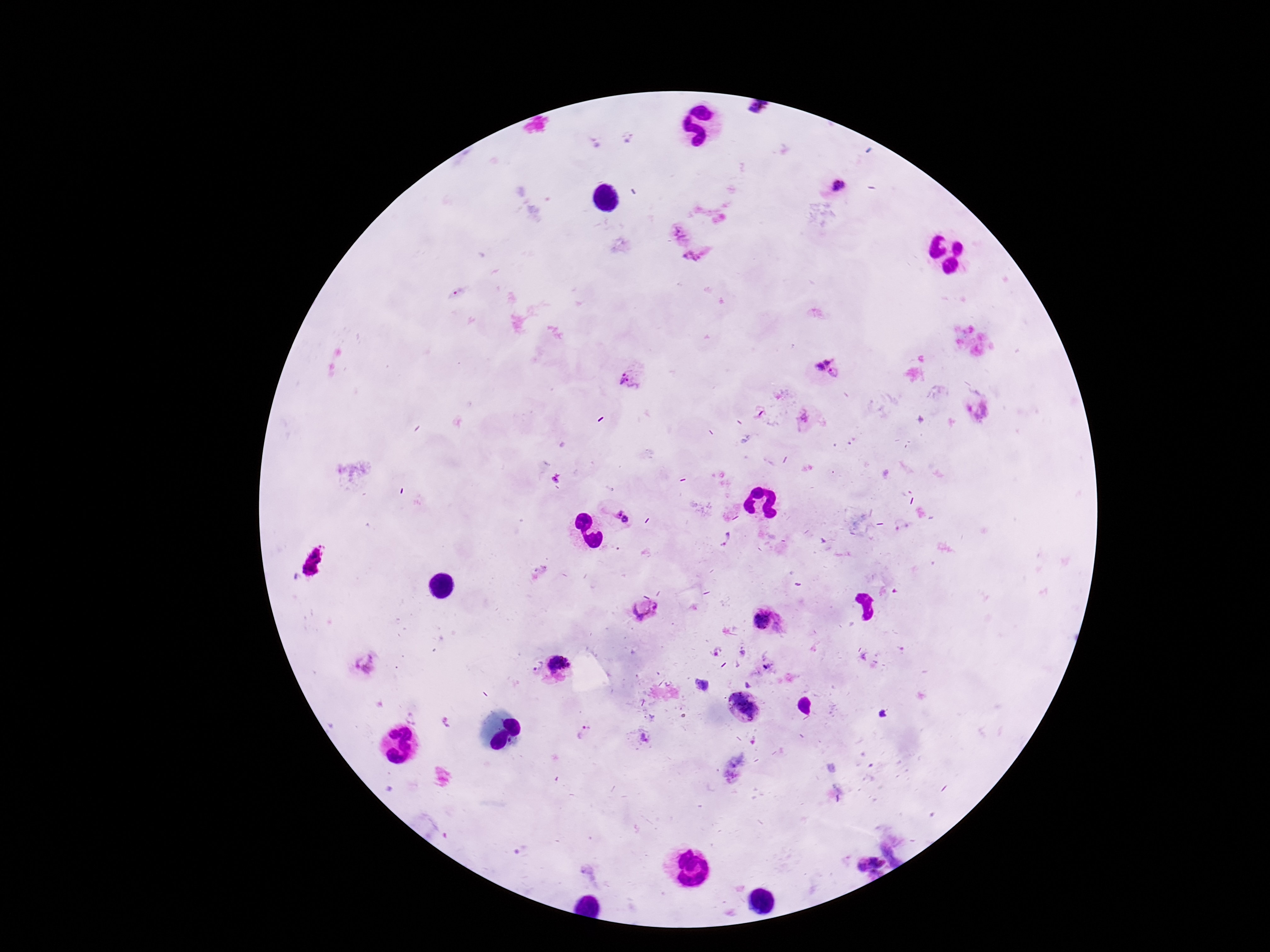

Approximate object centers, in pixels from the top-left corner. Plasmodium parasite locations: (x=836, y=186), (x=678, y=234), (x=697, y=259), (x=817, y=359), (x=838, y=374), (x=632, y=384), (x=805, y=419), (x=620, y=513), (x=644, y=609), (x=767, y=621), (x=365, y=664), (x=559, y=665), (x=531, y=666), (x=743, y=706), (x=586, y=734), (x=643, y=740), (x=867, y=860). Smartphone photograph taken through the microscope eyepiece. Thick peripheral-blood smear. Giemsa stain. 100x magnification. Patient malaria status: infected. One field from this slide. Image is 1270×952 pixels.